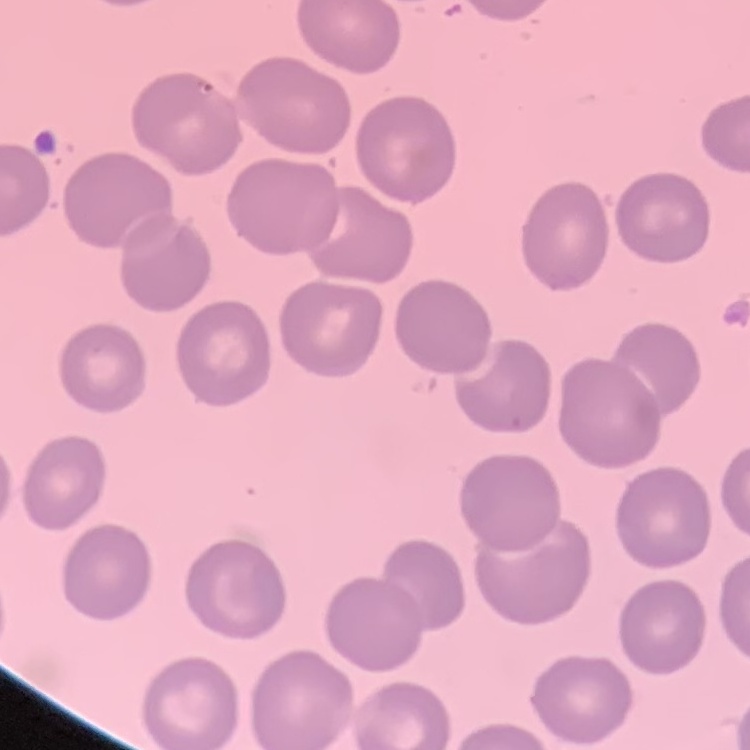

Summary:
  - Erythrocyte morphology: no rouleaux formation
  - Stain: Field's or Giemsa
  - Preparation: thin peripheral smear
  - Image type: square crop of a larger photomicrograph